Report the malaria status of this cell.
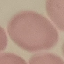

It is uninfected.

Summary:
  - Image type: cell patch, automatically extracted from a larger field of view and resized to 64 × 64 pixels
  - Capture: smartphone camera at the microscope eyepiece
  - Stain: Giemsa
  - Preparation: thin smear